Point out each Plasmodium parasite.
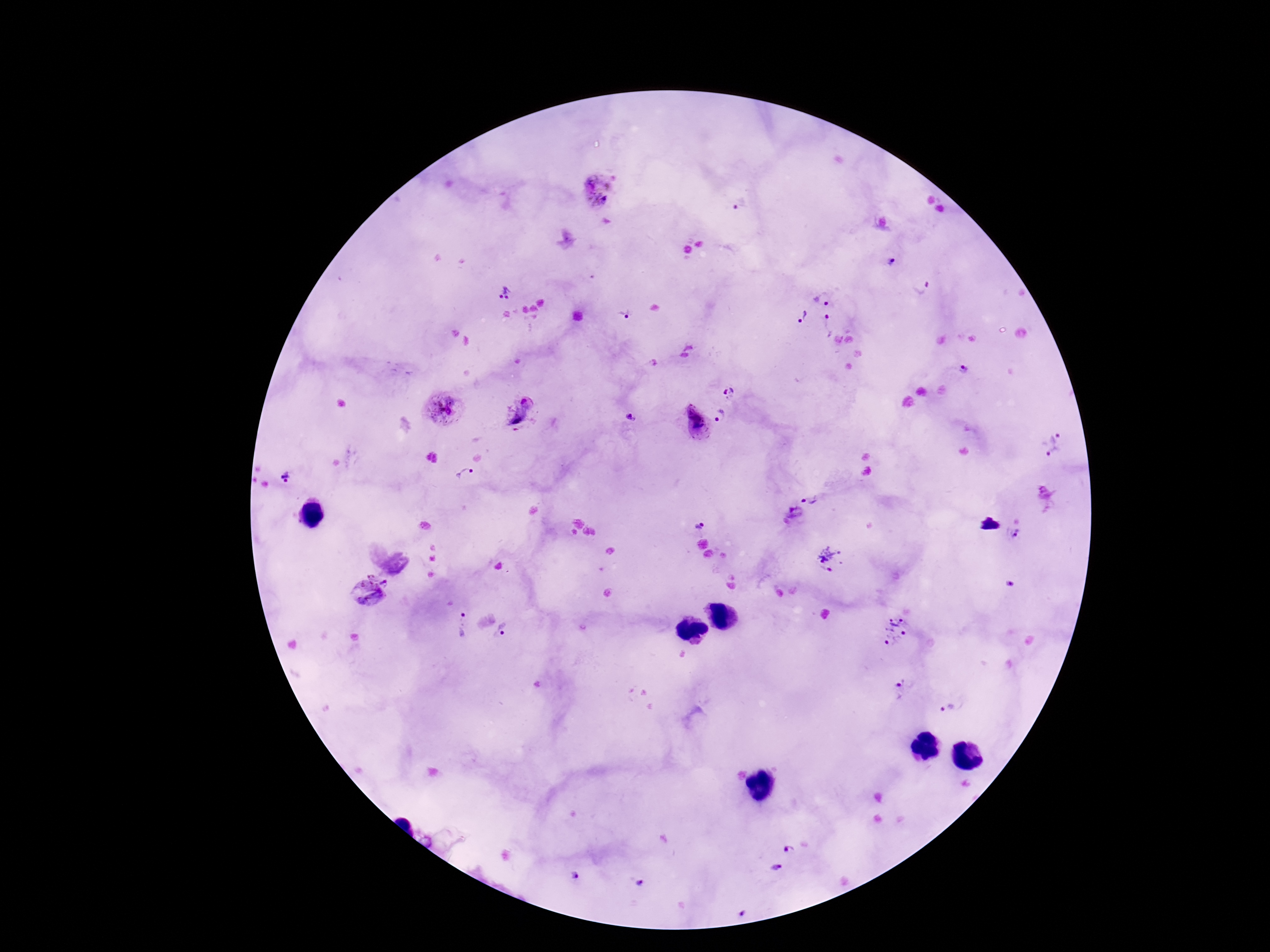
Approximate centers as (x, y) in pixels.
Plasmodium parasites: (598, 189), (740, 205), (891, 263), (922, 286), (504, 293), (823, 298), (626, 314), (802, 317), (829, 326), (964, 367), (729, 392), (442, 410), (518, 410), (721, 416), (630, 418), (695, 424), (1051, 445), (464, 475), (286, 478), (813, 497), (795, 514), (698, 526), (1015, 535), (832, 559), (377, 581), (1010, 584), (368, 593), (461, 623), (503, 631), (895, 631), (902, 688), (947, 709), (428, 841), (789, 850), (776, 867), (575, 876), (640, 883), (741, 913).

preparation = thick peripheral-blood smear
patient malaria status = positive
field of view = single
magnification = 100x
capture = smartphone camera through the microscope eyepiece
stain = Giemsa
image size = 1270×952 pixels